Comment on the morphology of the erythrocytes.
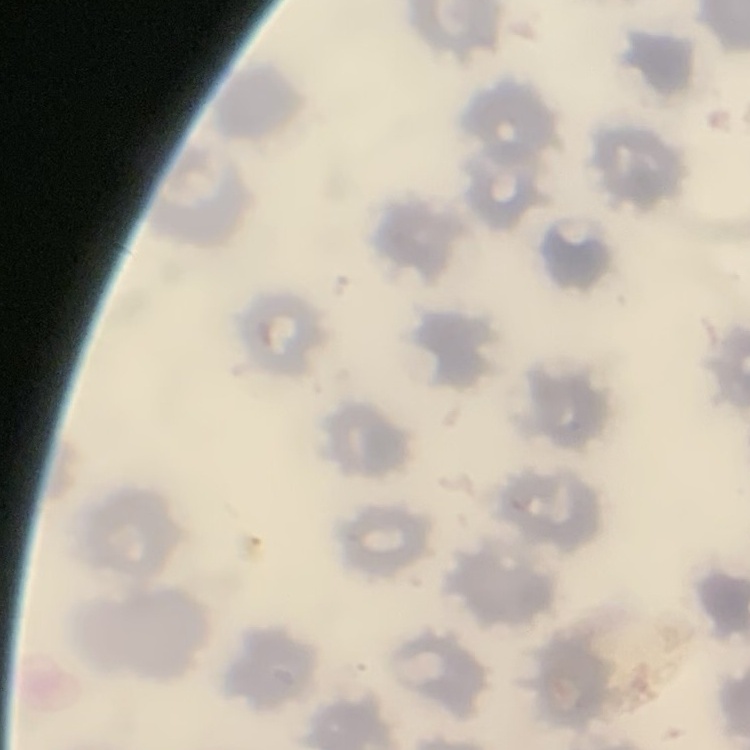

No rouleaux formation.

preparation = thin blood smear
image type = square crop of a larger photomicrograph
stain = Field's or Giemsa